Assess the morphology of the red blood cells.
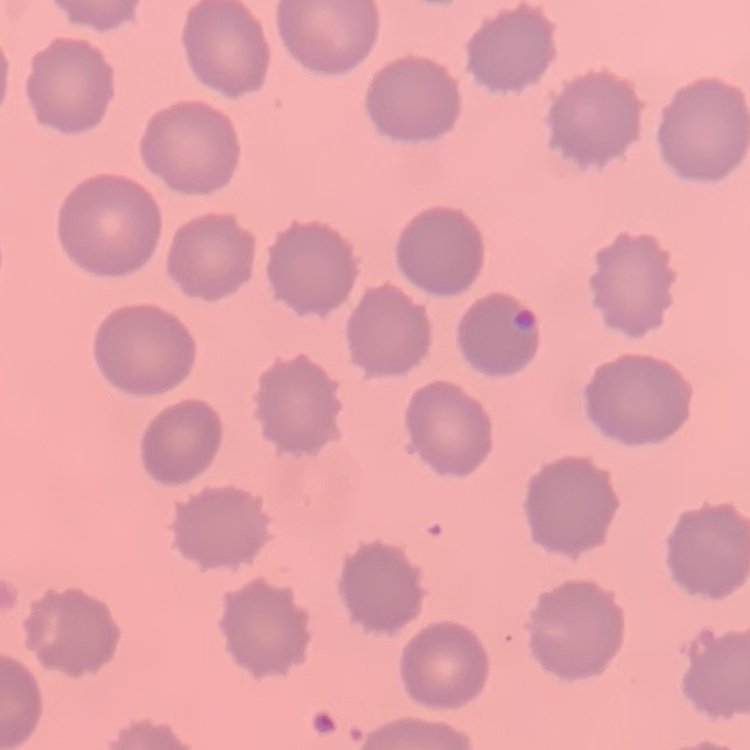

They show no rouleaux formation.

Summary:
  - Preparation: thin blood film
  - Stain: Field's or Giemsa
  - Image type: square crop of a larger photomicrograph